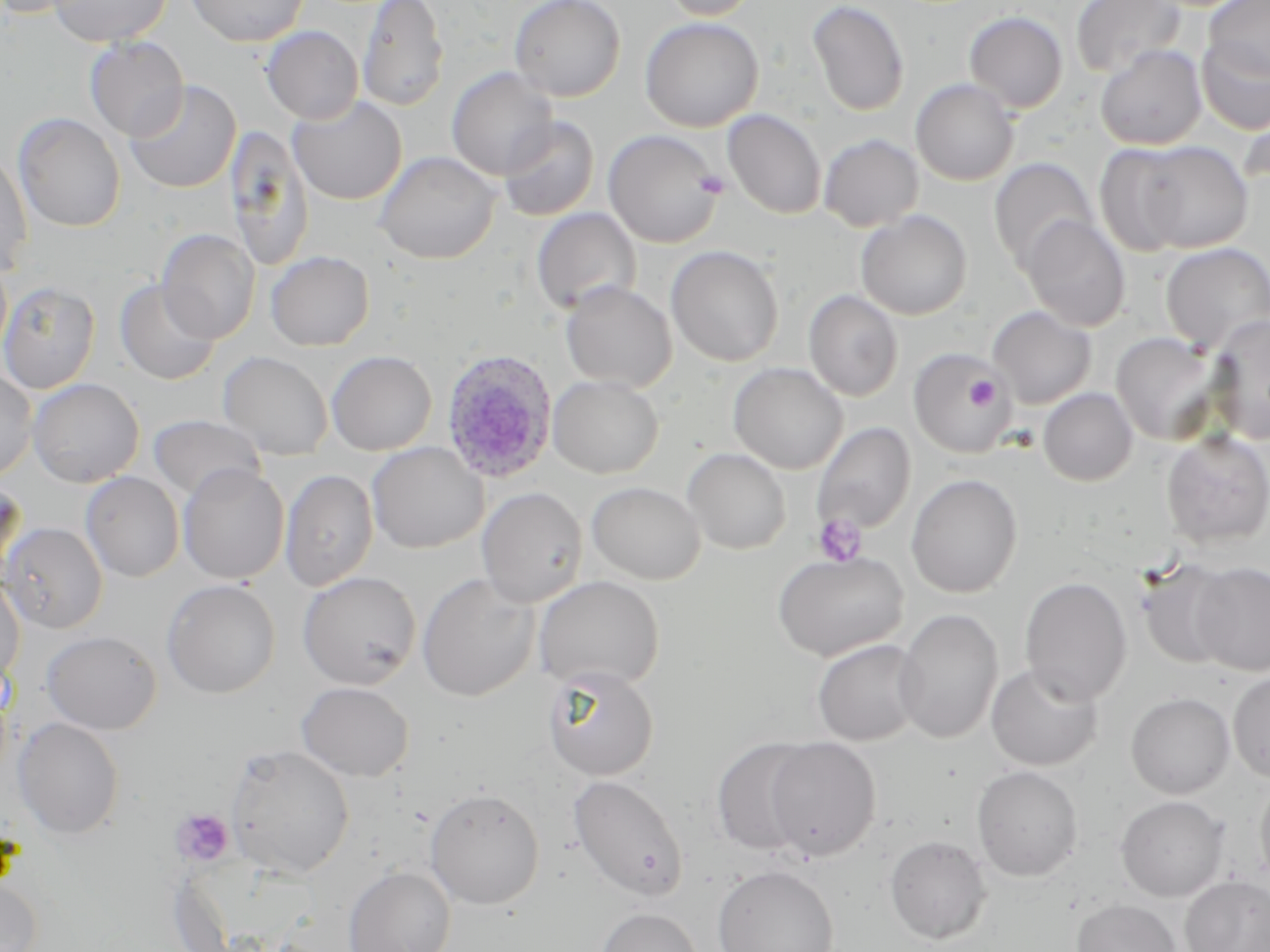
Summary:
  - Coordinate format: approximate bounding boxes as (x1, y1, x2, y2) in pixels
  - Plasmodium ovale-infected red blood cell locations: (440, 347, 558, 484)
  - Uninfected red blood cell locations: (0, 0, 90, 19), (49, 0, 171, 47), (186, 0, 310, 47), (357, 0, 449, 112), (509, 0, 626, 102), (659, 0, 761, 20), (1070, 0, 1185, 79), (1204, 0, 1270, 83), (807, 1, 909, 116), (964, 11, 1068, 113), (640, 17, 763, 132), (261, 25, 363, 124), (84, 36, 188, 141), (1196, 36, 1270, 135), (1095, 45, 1206, 150), (447, 67, 558, 179), (911, 79, 1019, 185), (124, 80, 241, 194), (288, 96, 407, 205), (723, 109, 827, 219), (13, 112, 125, 233), (499, 116, 599, 221), (225, 124, 314, 273), (603, 130, 724, 248), (818, 134, 924, 231), (1131, 140, 1253, 253), (1094, 144, 1191, 256), (0, 149, 33, 278), (374, 150, 502, 264), (989, 158, 1098, 270), (531, 208, 641, 315), (855, 210, 972, 320), (1020, 215, 1130, 332), (157, 229, 260, 344), (1160, 243, 1270, 352), (666, 245, 785, 367), (266, 250, 375, 351), (115, 279, 221, 385), (0, 280, 101, 394), (560, 281, 678, 392), (803, 290, 903, 401), (988, 306, 1096, 408), (1205, 313, 1270, 444), (1110, 331, 1224, 446), (908, 348, 1016, 459), (326, 350, 437, 456), (218, 351, 333, 460), (729, 363, 848, 474), (0, 367, 37, 482), (547, 375, 663, 478), (27, 378, 144, 487), (1038, 387, 1137, 486), (149, 414, 264, 502), (812, 422, 916, 535), (1161, 431, 1270, 547), (367, 442, 488, 553), (682, 448, 791, 555), (178, 463, 289, 584), (279, 469, 379, 591), (80, 471, 185, 582), (906, 473, 1023, 597), (0, 479, 26, 586), (587, 481, 705, 584), (477, 486, 588, 607), (1, 522, 108, 633), (773, 550, 908, 661), (1137, 559, 1236, 669), (1191, 561, 1270, 676), (298, 571, 421, 689), (0, 573, 25, 689), (417, 573, 540, 702), (534, 575, 665, 692), (1020, 576, 1132, 704), (161, 579, 281, 698), (894, 608, 1003, 744), (42, 630, 161, 734), (812, 639, 926, 746), (986, 662, 1104, 770), (543, 665, 659, 781), (1227, 670, 1270, 782), (296, 681, 414, 781), (1125, 692, 1235, 799), (13, 717, 125, 839), (711, 737, 818, 857), (762, 737, 882, 861), (226, 745, 355, 878), (972, 765, 1084, 881), (1254, 772, 1270, 890), (568, 774, 689, 901), (424, 788, 545, 909), (1115, 795, 1230, 902), (885, 835, 992, 944), (712, 864, 839, 952), (343, 865, 456, 952), (1180, 875, 1270, 952), (0, 877, 43, 952), (1072, 899, 1182, 952), (595, 907, 703, 952)
  - Platelet locations: (695, 170, 730, 199), (966, 376, 999, 410), (813, 514, 866, 566), (170, 809, 235, 867)
  - Slide-level diagnosis: Plasmodium ovale
  - Preparation: thin blood smear
  - Image size: 1270×952 pixels
  - Field of view: one of a larger specimen
  - Stain: May-Grünwald-Giemsa
  - Modality: optical microscopy
  - Magnification: 1000x